Classify this cell by malaria status.
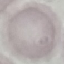

It is uninfected.

stain = Giemsa
image type = automatically extracted cell patch, resized to 64 × 64 pixels
preparation = thin blood smear
capture = smartphone through the microscope eyepiece